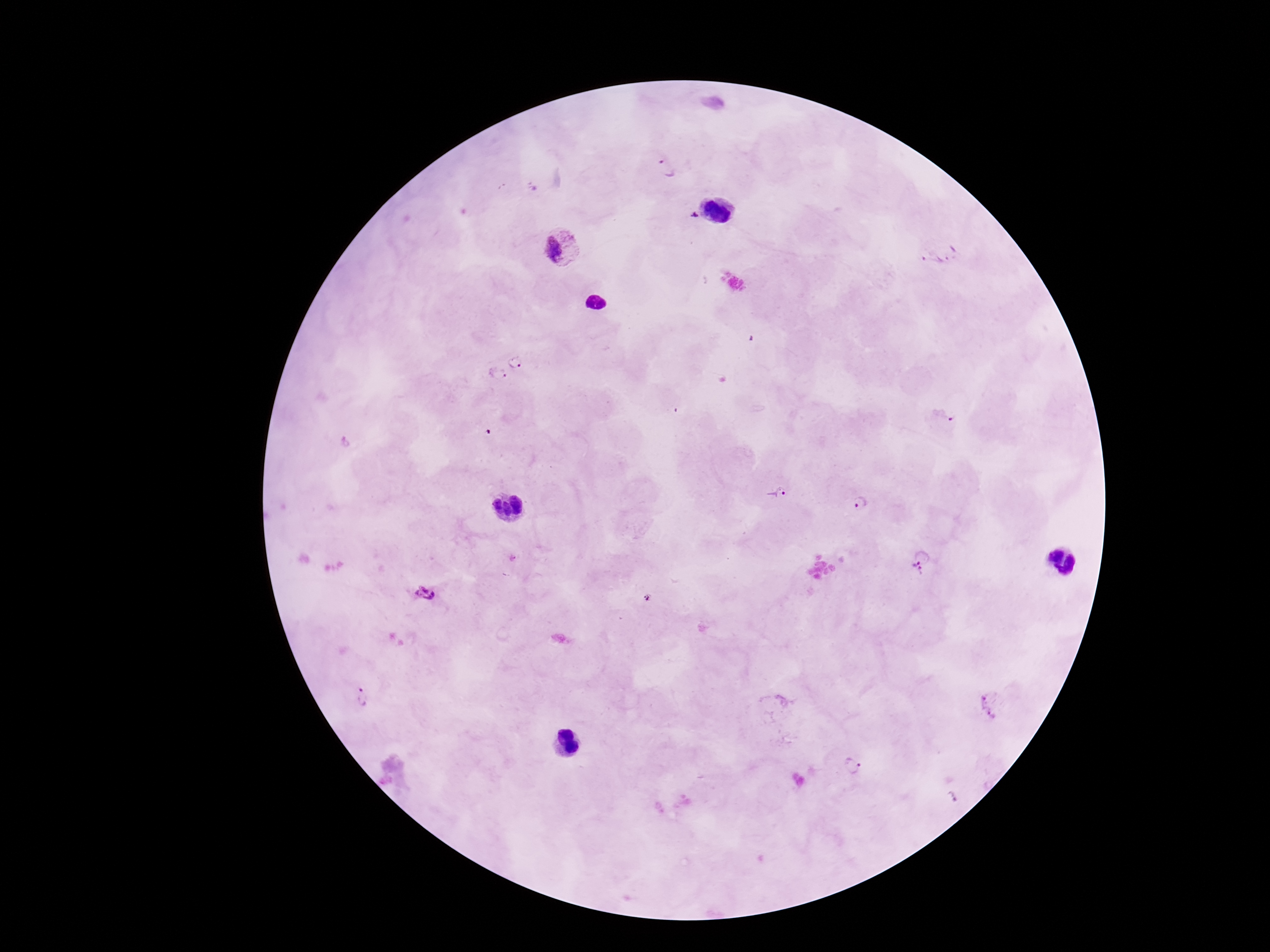

Approximate centers as (x, y) in pixels.
Summary:
  - Plasmodium parasite locations: (666, 167), (694, 215), (562, 246), (940, 252), (517, 361), (497, 376), (943, 416), (777, 492), (860, 502), (916, 570), (426, 592), (361, 697), (993, 703), (853, 767)
  - Magnification: 100x
  - Field of view: one from this slide
  - Stain: Giemsa
  - Patient malaria status: positive
  - Preparation: thick blood smear
  - Capture: smartphone camera through the microscope eyepiece
  - Image size: 1270×952 pixels